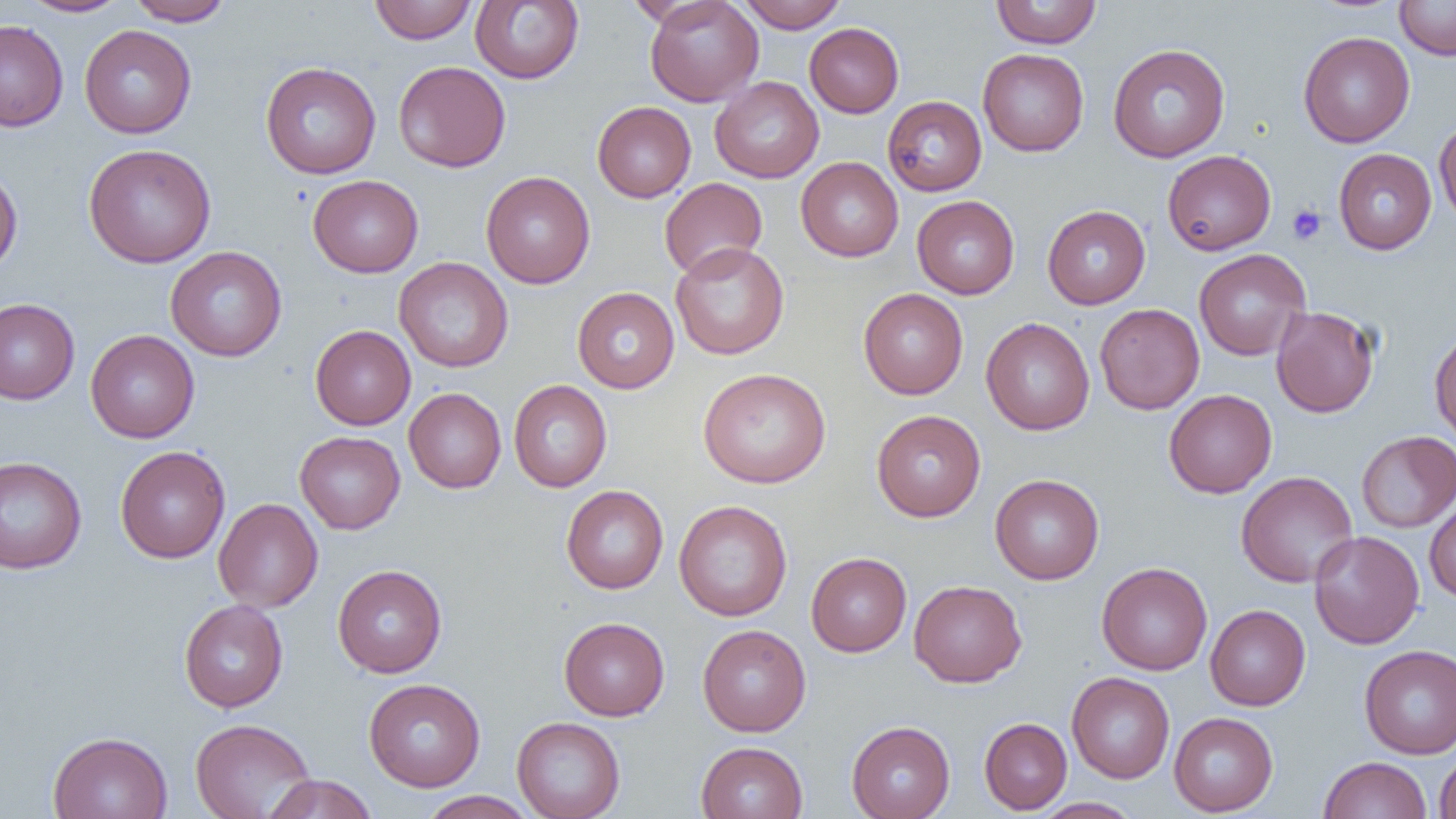

Approximate bounding boxes as (x1, y1, x2, y2) in pixels. Uninfected red blood cell locations: (19, 0, 131, 17), (126, 0, 232, 26), (369, 0, 477, 44), (644, 0, 763, 106), (736, 0, 849, 32), (990, 0, 1102, 49), (1394, 0, 1456, 60), (470, 1, 584, 84), (0, 19, 68, 132), (805, 23, 903, 117), (79, 25, 197, 138), (1298, 31, 1415, 148), (1107, 43, 1230, 162), (978, 49, 1089, 156), (393, 60, 511, 172), (260, 61, 381, 179), (710, 76, 824, 183), (883, 96, 987, 196), (592, 101, 696, 202), (1434, 117, 1456, 229), (83, 143, 216, 268), (1334, 148, 1437, 254), (1162, 149, 1276, 255), (796, 157, 903, 262), (0, 165, 23, 275), (480, 171, 595, 289), (308, 175, 423, 278), (659, 177, 767, 280), (912, 195, 1019, 298), (1042, 205, 1150, 309), (670, 242, 789, 360), (165, 246, 287, 362), (1194, 249, 1311, 361), (394, 258, 513, 372), (572, 287, 679, 393), (858, 288, 968, 399), (0, 299, 80, 404), (1094, 303, 1205, 414), (1271, 305, 1380, 418), (981, 317, 1094, 435), (310, 325, 416, 430), (1429, 328, 1456, 447), (85, 330, 200, 443), (698, 368, 831, 487), (508, 380, 612, 492), (404, 387, 506, 493), (1164, 389, 1277, 498), (871, 410, 986, 522), (295, 431, 405, 534), (1356, 431, 1456, 532), (115, 445, 230, 563), (0, 456, 87, 574), (1235, 471, 1359, 588), (990, 474, 1104, 585), (561, 485, 668, 594), (1424, 493, 1456, 602), (213, 498, 323, 612), (674, 500, 792, 621), (1309, 530, 1424, 649), (806, 552, 911, 657), (1097, 562, 1213, 675), (332, 564, 447, 678), (909, 580, 1027, 687), (179, 599, 288, 712), (1206, 604, 1310, 711), (558, 617, 669, 721), (697, 624, 811, 736), (1359, 645, 1456, 758), (1067, 672, 1175, 783), (364, 678, 486, 792), (1169, 711, 1278, 816), (512, 716, 625, 819), (979, 717, 1072, 814), (190, 718, 315, 819), (846, 720, 955, 819), (48, 731, 173, 819), (696, 741, 808, 819), (1434, 749, 1456, 818), (1318, 756, 1432, 819), (261, 774, 378, 819), (418, 790, 537, 819), (1032, 797, 1141, 818). Platelet locations: (1287, 203, 1327, 245). Slide-level diagnosis: negative for blood parasites. Image is 1456×819 pixels. Captured at 1000x magnification. Thin blood smear. Single field of view. Light microscopy.